Comment on the background quality.
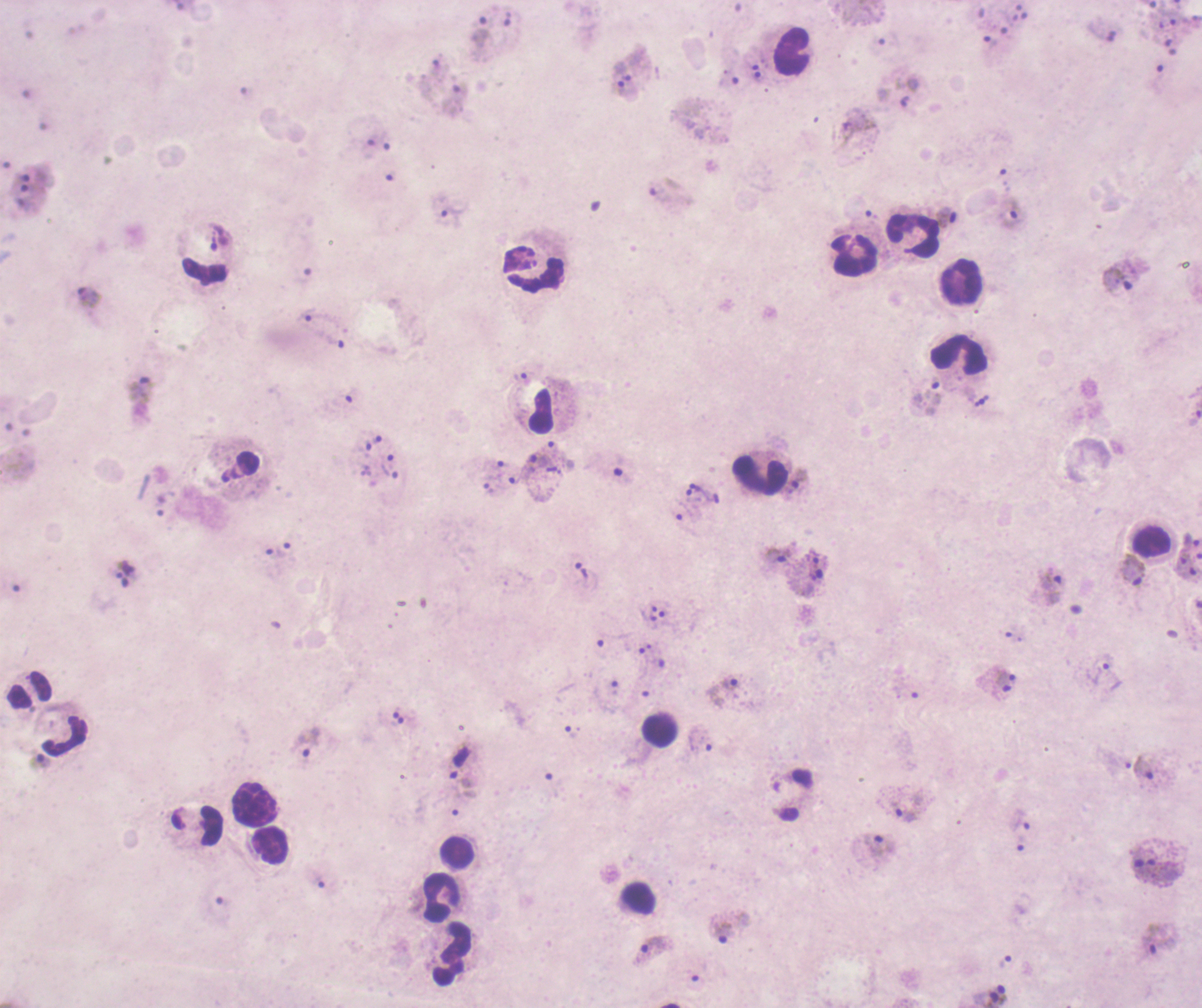
Unsatisfactory.

Approximate centers as [x, y] in pixels. Trophozoite locations: [480, 31], [992, 48], [623, 71], [628, 91], [858, 124], [1011, 213], [448, 214], [947, 218], [1117, 278], [88, 298], [319, 314], [330, 339], [141, 389], [933, 392], [541, 470], [388, 472], [701, 490], [775, 555], [582, 571], [1131, 571], [1049, 586], [1098, 670], [724, 691], [306, 742], [39, 762], [1142, 769], [904, 812], [1020, 822], [877, 850], [721, 930], [1156, 939], [651, 949]. Leukocyte locations: [791, 51], [912, 235], [854, 254], [202, 269], [539, 277], [960, 282], [959, 354], [542, 411], [760, 477], [1149, 543], [30, 691], [658, 730], [67, 734], [255, 803], [269, 846], [457, 851], [636, 898], [440, 899], [451, 955]. Coloration quality: bad. Result: Plasmodium parasites identified. Romanowsky-stained preparation. Single field of view. Captured at 100x magnification. Thick smear of blood. Image is 1202×1008 pixels. Previously used in an actual diagnosis.